Name the blood parasite species.
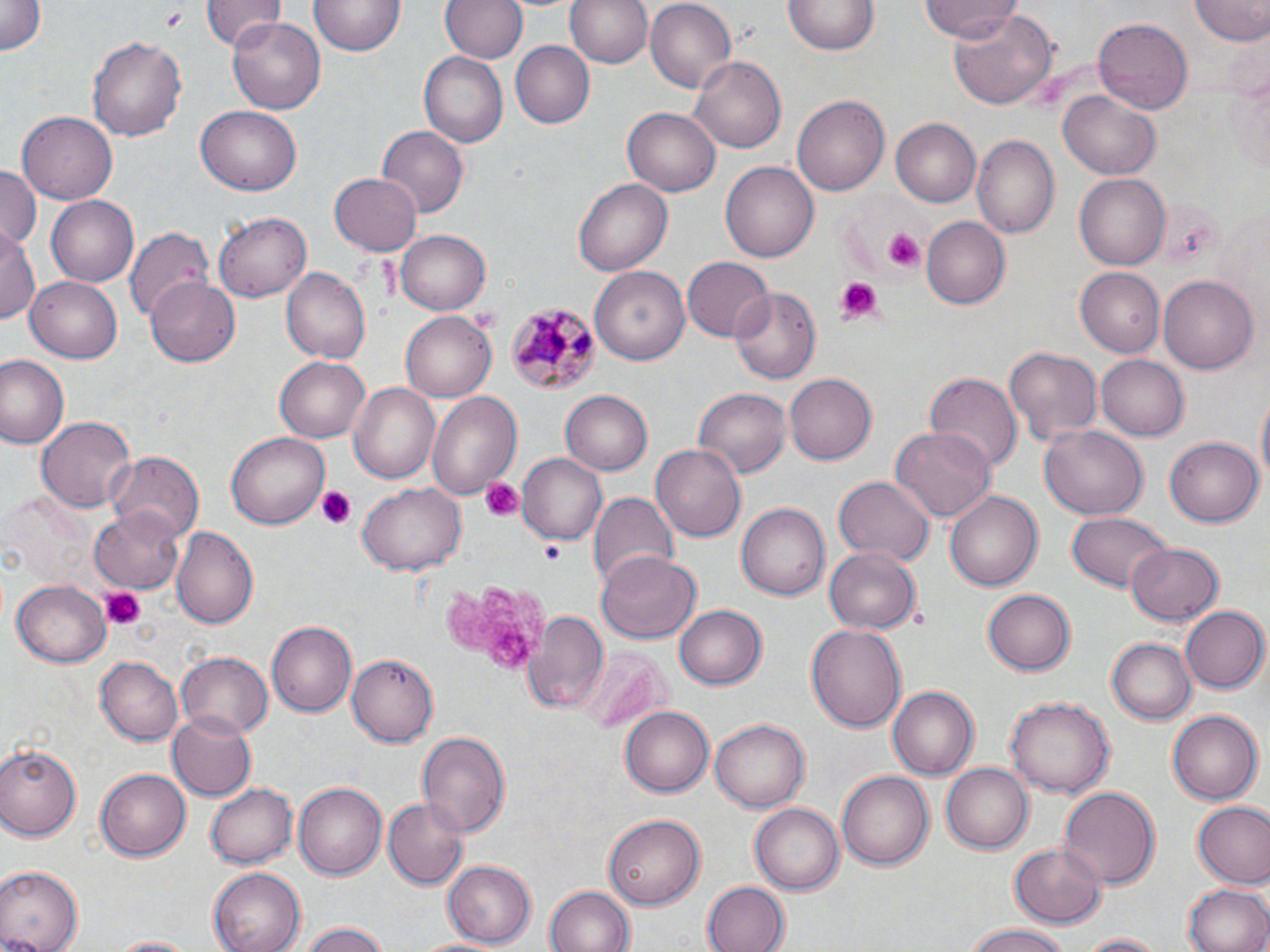
Plasmodium malariae.

magnification: 1000x
plasmodium_malariae_infected_red_blood_cell_locations: 'approximate bounding boxes as [x1, y1, x2, y2] in pixels: [505, 300, 599, 395]'
stain: May-Grünwald-Giemsa
preparation: thin blood smear
platelet_locations: 'approximate bounding boxes as [x1, y1, x2, y2] in pixels: [881, 227, 925, 275], [831, 278, 883, 328], [468, 304, 504, 334], [480, 478, 522, 522], [316, 486, 356, 530], [446, 577, 553, 677], [99, 587, 143, 629]'
image_size: 1270×952 pixels
uninfected_red_blood_cell_locations: 'approximate bounding boxes as [x1, y1, x2, y2] in pixels: [203, 0, 284, 50], [441, 0, 527, 65], [566, 0, 653, 70], [643, 0, 736, 93], [311, 1, 404, 57], [1189, 1, 1270, 45], [0, 2, 46, 57], [783, 2, 878, 56], [924, 2, 1020, 44], [947, 6, 1057, 111], [1092, 17, 1193, 112], [229, 18, 327, 115], [89, 34, 185, 145], [510, 40, 593, 130], [1227, 51, 1268, 179], [420, 53, 508, 147], [690, 55, 785, 154], [1059, 92, 1161, 180], [792, 94, 889, 196], [195, 107, 301, 196], [624, 107, 719, 196], [16, 110, 119, 204], [891, 117, 983, 208], [375, 126, 467, 218], [972, 136, 1060, 237], [720, 161, 819, 261], [0, 164, 40, 246], [329, 172, 422, 255], [1074, 172, 1169, 271], [575, 178, 673, 275], [46, 196, 138, 285], [215, 212, 312, 301], [919, 214, 1010, 310], [0, 224, 38, 327], [124, 228, 212, 329], [394, 230, 491, 316], [681, 257, 773, 342], [590, 263, 688, 364], [280, 266, 370, 364], [1074, 268, 1164, 356], [1160, 274, 1258, 374], [25, 277, 122, 363], [146, 279, 242, 367], [729, 286, 821, 385], [401, 312, 496, 402], [1002, 342, 1104, 448], [1098, 355, 1190, 440], [0, 356, 69, 451], [275, 357, 369, 443], [927, 371, 1021, 477], [785, 373, 877, 465], [348, 382, 442, 484], [692, 388, 788, 479], [425, 390, 522, 499], [561, 391, 652, 474], [36, 415, 136, 513], [1041, 425, 1149, 520], [890, 426, 995, 523], [227, 432, 329, 529], [1165, 436, 1262, 528], [652, 446, 745, 541], [106, 450, 202, 540], [517, 454, 609, 545], [835, 476, 933, 567], [357, 483, 466, 576], [2, 492, 92, 586], [946, 492, 1042, 592], [589, 493, 677, 585], [737, 503, 829, 601], [92, 506, 187, 594], [1066, 512, 1171, 594], [171, 527, 259, 630], [1125, 543, 1225, 624], [825, 545, 922, 635], [597, 551, 698, 642], [11, 577, 113, 665], [982, 589, 1075, 677], [674, 605, 767, 690], [1182, 605, 1270, 693], [524, 608, 607, 712], [267, 620, 357, 717], [806, 624, 909, 733], [1107, 636, 1195, 722], [176, 651, 273, 738], [582, 651, 670, 734], [347, 654, 438, 747], [95, 657, 181, 745], [887, 687, 977, 779], [1004, 693, 1113, 797], [621, 705, 717, 797], [1167, 709, 1261, 805], [168, 710, 257, 801], [710, 717, 810, 811], [419, 733, 509, 841], [2, 745, 82, 839], [943, 764, 1033, 853], [97, 767, 193, 862], [835, 770, 934, 871], [204, 782, 294, 870], [295, 782, 387, 879], [1059, 786, 1161, 890], [381, 798, 464, 888], [1192, 802, 1270, 887], [751, 803, 843, 895], [604, 814, 706, 908], [1009, 841, 1105, 926], [441, 861, 537, 945], [0, 865, 83, 952], [207, 868, 305, 952], [702, 881, 788, 952], [1184, 884, 1269, 952], [545, 886, 635, 952], [962, 922, 1076, 952], [301, 925, 390, 952], [1070, 932, 1175, 951], [413, 934, 508, 952], [107, 935, 201, 952]'
field_of_view: single
modality: optical microscopy